Assess this cell for malaria.
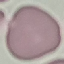

It is uninfected.

Summary:
  - Capture: smartphone through the microscope eyepiece
  - Image type: cell patch, automatically extracted from a larger field of view and resized to 64 × 64 pixels
  - Stain: Giemsa
  - Preparation: thin blood film